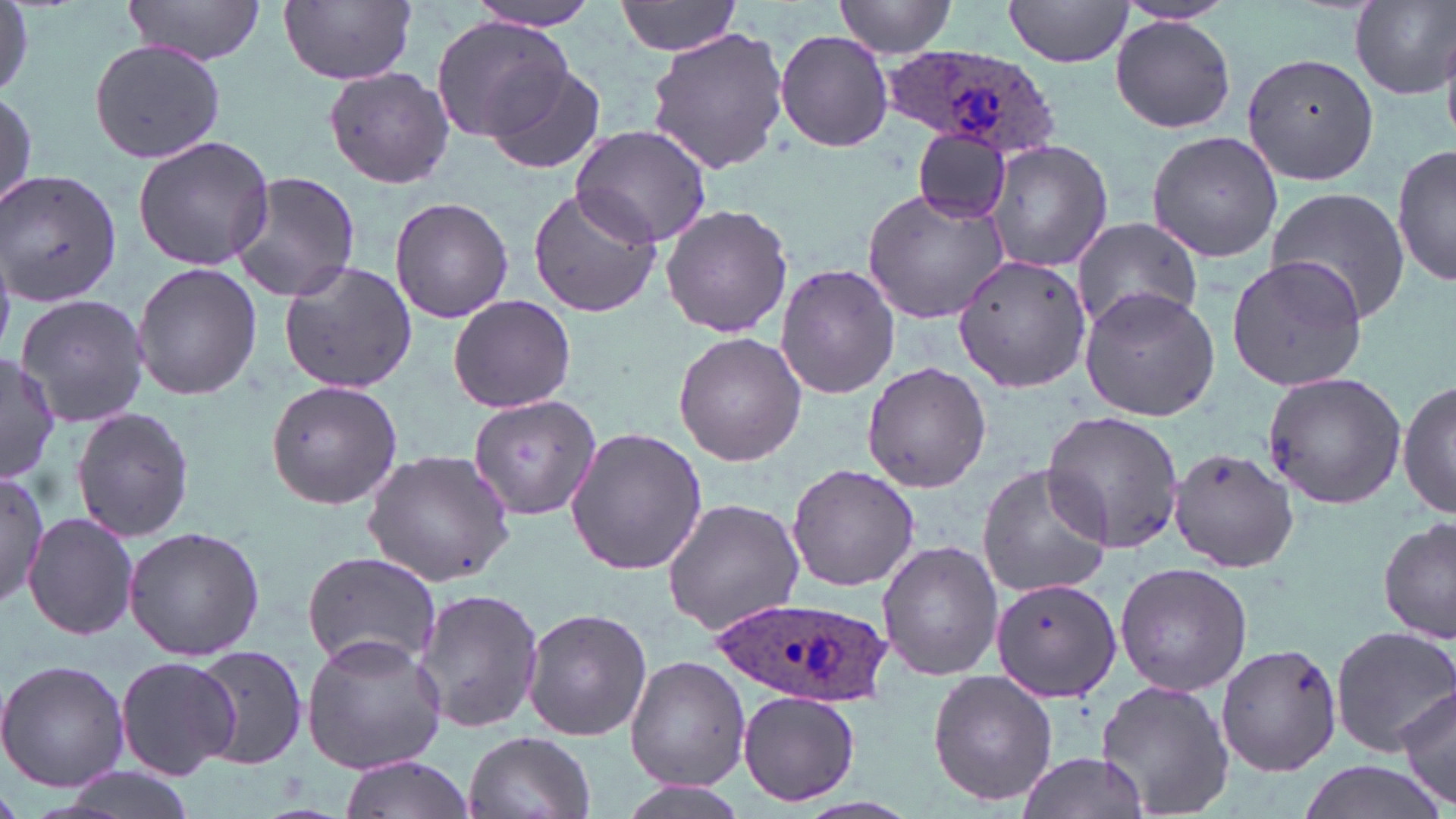 Approximate bounding boxes as (x1, y1, x2, y2) in pixels. Plasmodium ovale-infected red blood cell locations: (888, 40, 1060, 165), (713, 593, 888, 708). Uninfected red blood cell locations: (120, 0, 267, 64), (279, 0, 417, 85), (615, 0, 741, 55), (834, 0, 957, 58), (1351, 0, 1455, 99), (1001, 1, 1137, 66), (460, 2, 602, 32), (1110, 16, 1237, 133), (430, 17, 569, 140), (644, 26, 792, 176), (774, 29, 894, 153), (87, 38, 226, 165), (1246, 51, 1385, 183), (475, 58, 608, 177), (324, 67, 455, 189), (0, 88, 37, 215), (571, 122, 714, 249), (911, 127, 1012, 224), (1144, 129, 1283, 263), (132, 134, 275, 272), (985, 139, 1111, 273), (1392, 143, 1454, 291), (0, 170, 123, 307), (227, 171, 362, 303), (526, 185, 663, 319), (1265, 185, 1411, 326), (862, 186, 1011, 323), (389, 196, 514, 321), (660, 204, 793, 339), (1068, 217, 1204, 335), (952, 253, 1092, 394), (1227, 253, 1371, 393), (277, 260, 418, 394), (131, 262, 263, 400), (774, 263, 901, 400), (1080, 288, 1220, 422), (15, 292, 152, 431), (447, 294, 577, 415), (672, 330, 807, 467), (0, 354, 59, 484), (862, 361, 993, 493), (1261, 370, 1410, 511), (265, 379, 405, 508), (1398, 379, 1456, 519), (468, 395, 601, 520), (71, 405, 195, 542), (1042, 410, 1185, 553), (563, 425, 707, 577), (1168, 446, 1299, 572), (363, 449, 517, 585), (785, 462, 920, 592), (976, 462, 1112, 601), (0, 467, 47, 616), (662, 497, 806, 636), (24, 510, 139, 643), (1379, 517, 1455, 646), (123, 526, 264, 660), (876, 538, 1003, 681), (302, 551, 444, 673), (1115, 561, 1251, 694), (988, 579, 1124, 700), (410, 588, 544, 734), (522, 607, 652, 741), (1329, 624, 1456, 756), (300, 633, 447, 774), (1213, 642, 1344, 777), (186, 643, 308, 770), (624, 654, 750, 791), (114, 655, 238, 779), (0, 658, 129, 792), (926, 669, 1058, 808), (1096, 676, 1235, 819), (1396, 683, 1456, 813), (736, 688, 861, 808), (463, 730, 595, 819), (1014, 750, 1152, 819), (338, 756, 477, 819), (1290, 760, 1449, 819), (43, 770, 200, 819). Slide-level diagnosis: Plasmodium ovale. May-Grünwald-Giemsa-stained preparation. 1000x magnification. Thin blood smear. Optical microscopy. Single field of view. Image is 1456×819 pixels.